State the blood parasite species.
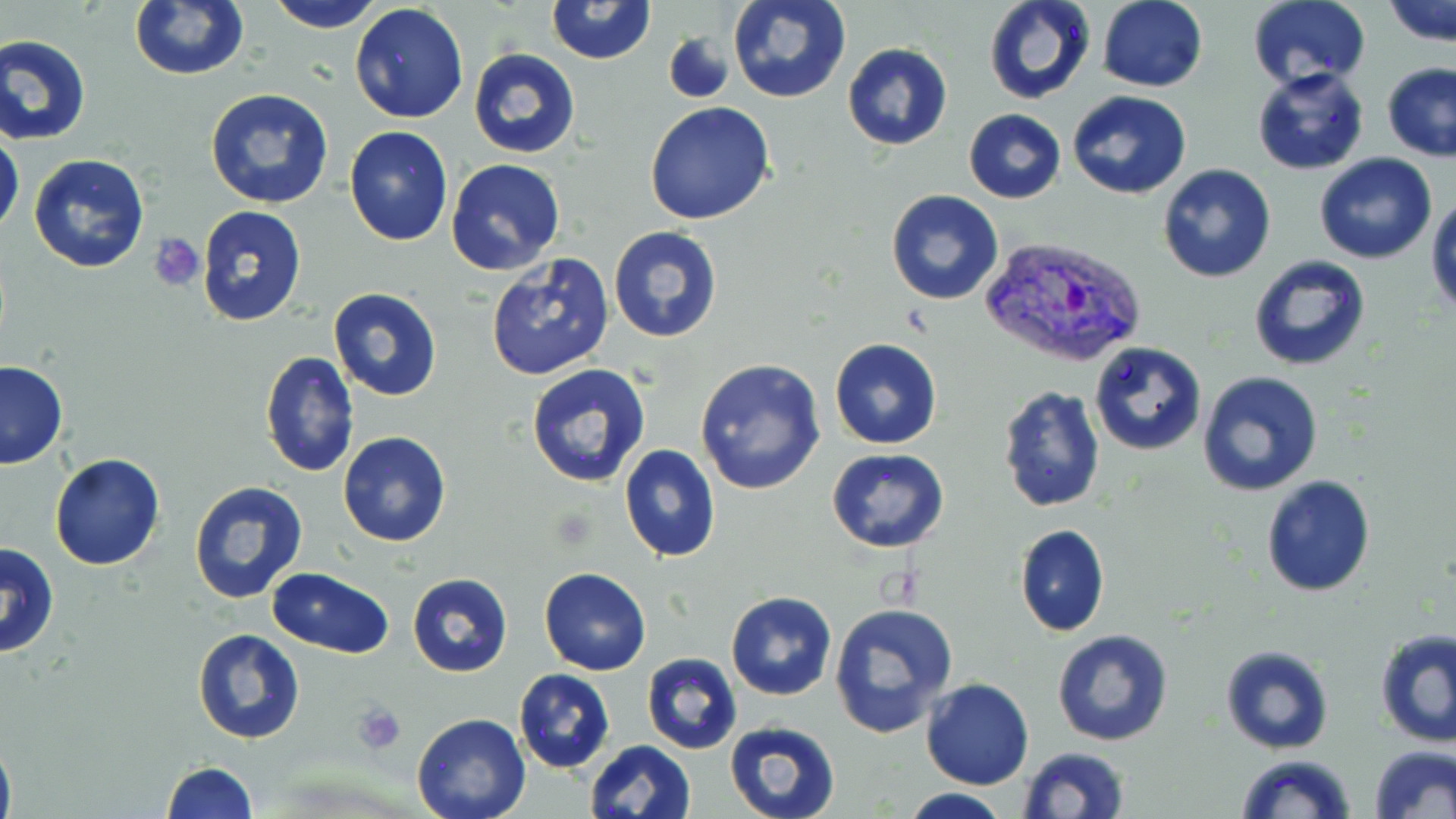
Plasmodium vivax.

field of view = one of a larger specimen
uninfected red blood cell locations = approximate bounding boxes as (x1,y1)-(x2,y2) corner pairs in pixels: (264,0)-(386,31), (546,0)-(655,65), (726,0)-(851,104), (984,0)-(1097,104), (1096,0)-(1208,92), (1244,0)-(1371,93), (1384,0)-(1456,49), (128,1)-(249,81), (349,4)-(470,123), (662,25)-(739,104), (0,33)-(93,146), (842,43)-(953,151), (466,48)-(581,161), (1381,62)-(1456,162), (1251,67)-(1370,177), (204,88)-(334,210), (1067,91)-(1192,201), (645,101)-(776,225), (964,110)-(1065,204), (344,126)-(453,246), (0,128)-(24,240), (1314,153)-(1437,264), (28,154)-(150,274), (445,159)-(566,278), (1155,163)-(1277,283), (885,189)-(1003,306), (1428,194)-(1456,315), (196,205)-(308,328), (607,227)-(725,344), (484,253)-(614,381), (1247,254)-(1372,373), (327,288)-(444,402), (829,339)-(942,449), (1089,342)-(1208,456), (259,350)-(359,478), (695,357)-(825,496), (0,361)-(69,470), (526,363)-(651,487), (1197,371)-(1324,498), (995,382)-(1106,514), (338,431)-(452,546), (620,445)-(721,562), (826,449)-(949,553), (48,455)-(165,572), (1260,474)-(1376,596), (187,480)-(309,603), (1015,523)-(1109,636), (1,541)-(61,657), (539,567)-(651,676), (269,569)-(395,659), (406,572)-(512,676), (726,591)-(837,701), (829,601)-(959,736), (192,629)-(306,745), (1374,629)-(1456,748), (1052,630)-(1175,747), (1220,644)-(1334,754), (642,654)-(741,755), (514,668)-(615,774), (921,679)-(1033,789), (410,714)-(529,819), (724,720)-(840,819), (0,732)-(15,819), (585,739)-(695,819), (1371,745)-(1456,819), (1017,746)-(1132,819), (1234,753)-(1356,819), (161,762)-(257,818), (900,789)-(1014,819)
Plasmodium vivax-infected red blood cell locations = approximate bounding boxes as (x1,y1)-(x2,y2) corner pairs in pixels: (981,235)-(1147,368)
modality = optical microscopy
platelet locations = approximate bounding boxes as (x1,y1)-(x2,y2) corner pairs in pixels: (152,234)-(205,290), (352,703)-(406,754)
magnification = 1000x
image size = 1456×819 pixels
preparation = thin blood smear
stain = May-Grünwald-Giemsa